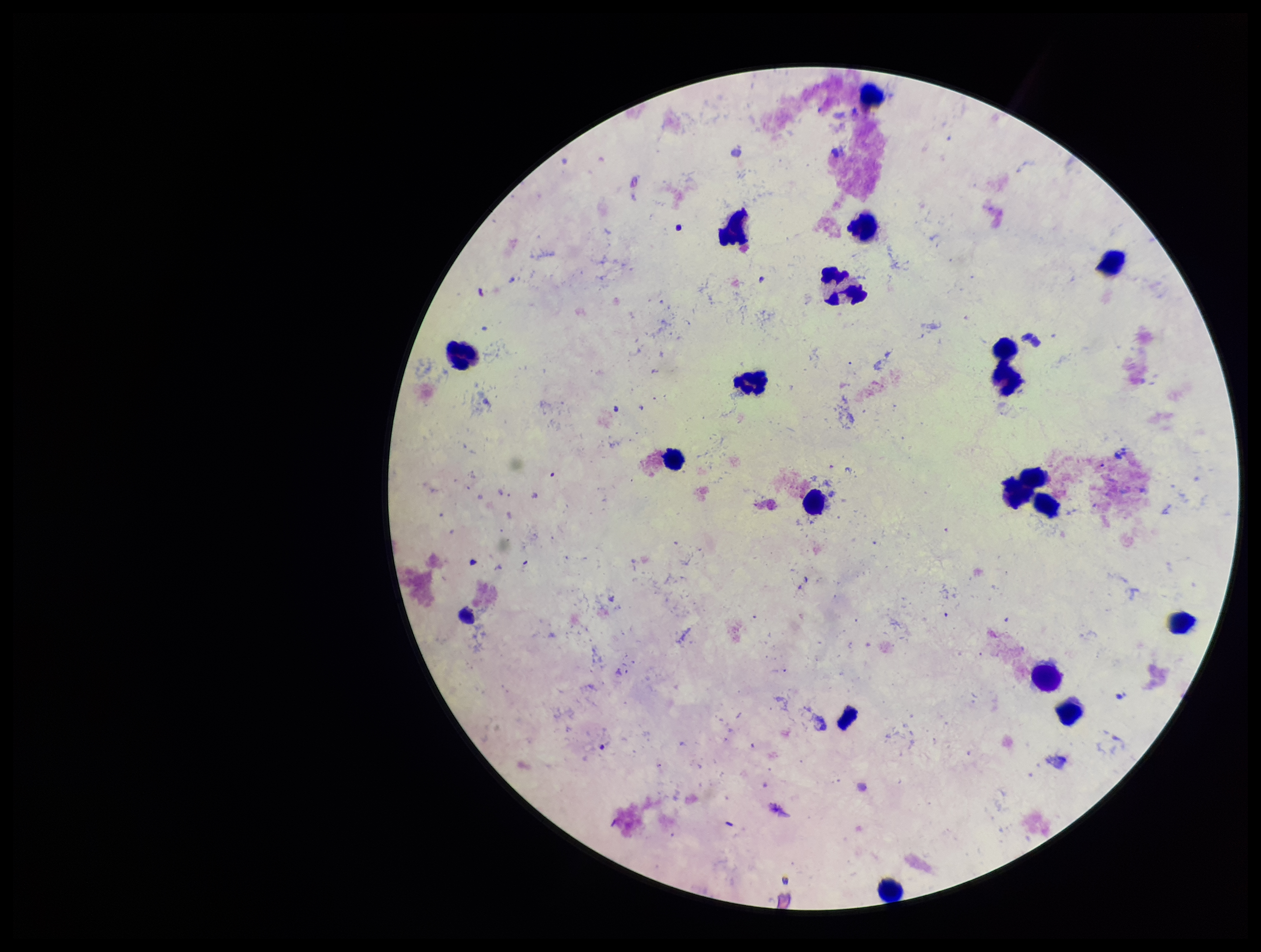
stain = Giemsa
capture = smartphone photograph through the microscope eyepiece
patient malaria status = negative
Plasmodium parasites = none identified
image size = 1261×952 pixels
field of view = one from this slide
leukocyte count = 16
preparation = thick
parasite count = 0